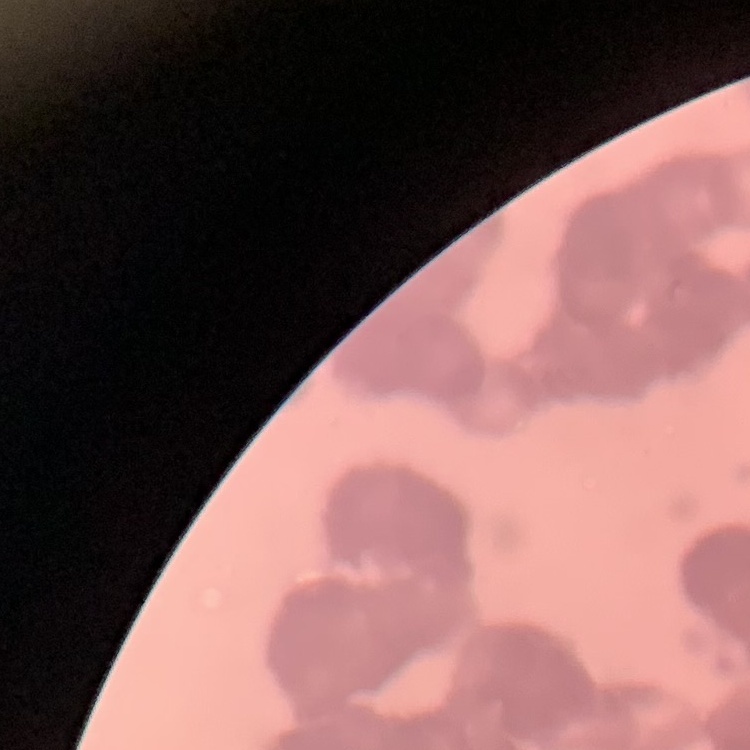 The red blood cells exhibit rouleaux formation. Square crop of a larger photomicrograph. Field's or Giemsa stain. Thin blood smear.